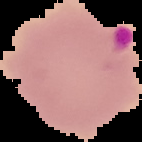
The area outside the segmented cell region is set to black. From a thin blood smear. Image is 142×142 pixels. Result: malaria parasites detected.